Look for Plasmodium parasites.
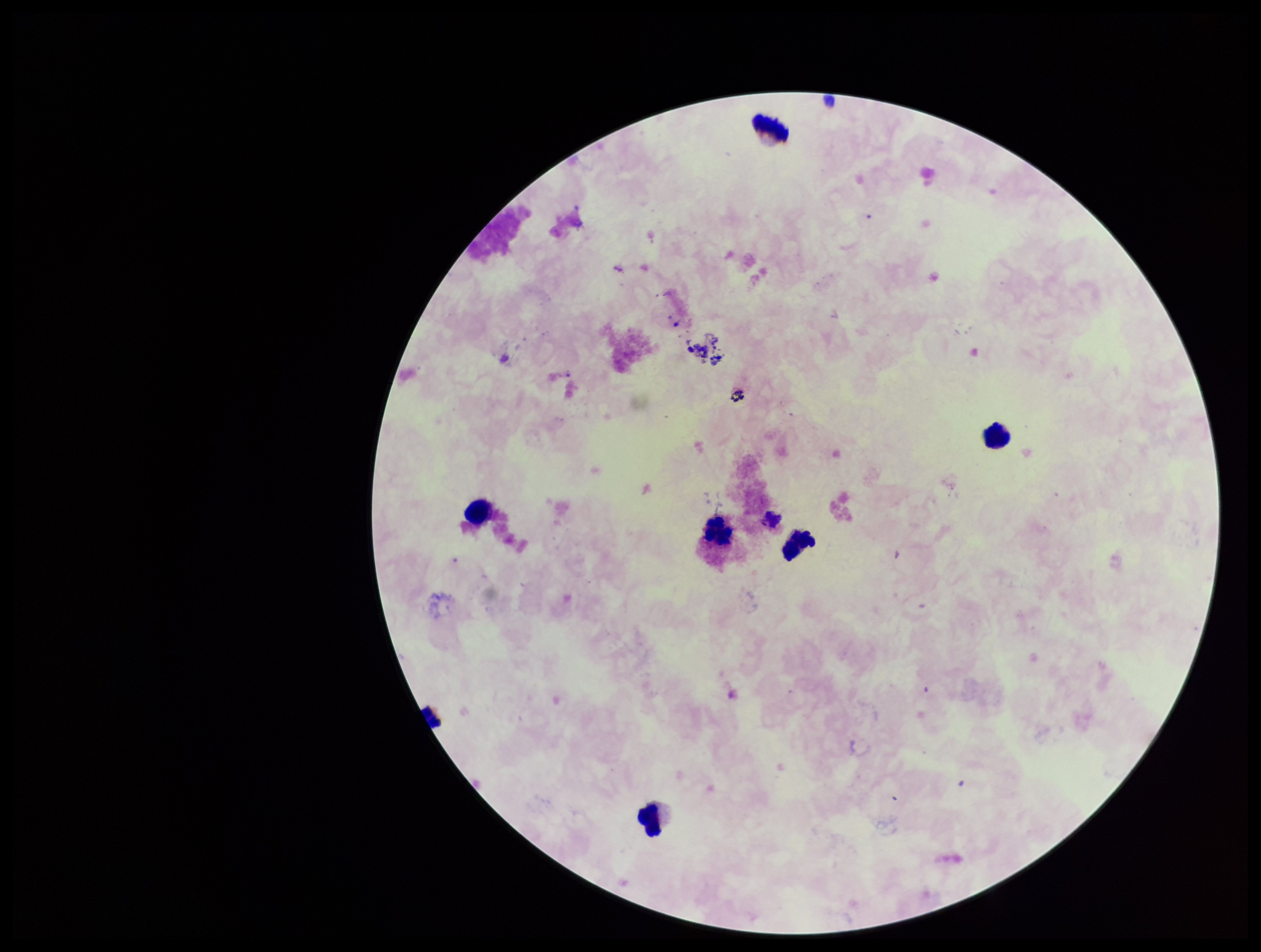
None identified.

stain = Giemsa
field of view = single
image size = 1261×952 pixels
capture = smartphone photograph through the microscope eyepiece
patient malaria status = negative
leukocyte count = 6
preparation = thick
parasite count = 0